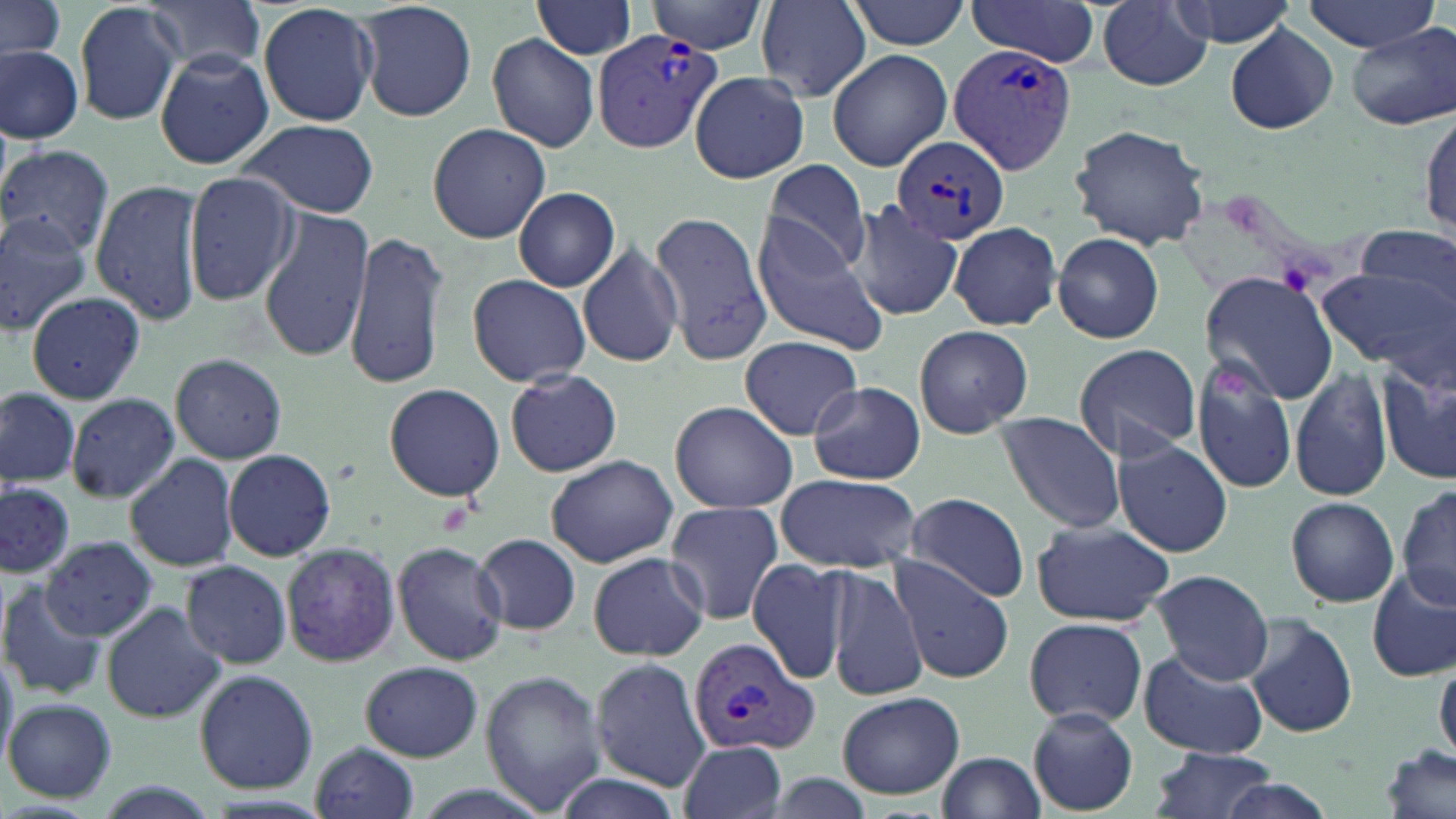

slide_level_diagnosis: Plasmodium vivax
stain: May-Grünwald-Giemsa
magnification: 1000x
preparation: thin blood film
uninfected_red_blood_cell_locations: 'approximate bounding boxes as (x1, y1, x2, y2) in pixels: (1, 0, 67, 63), (354, 0, 477, 121), (756, 0, 872, 100), (1166, 0, 1298, 47), (75, 1, 184, 126), (534, 1, 639, 60), (647, 1, 768, 52), (847, 1, 973, 51), (963, 1, 1103, 66), (1092, 1, 1217, 92), (1301, 1, 1440, 53), (145, 2, 266, 75), (258, 2, 379, 128), (92, 22, 232, 161), (1225, 23, 1339, 134), (1348, 26, 1455, 128), (487, 33, 599, 152), (1, 45, 83, 143), (826, 47, 951, 173), (155, 50, 273, 168), (690, 71, 809, 184), (1418, 105, 1455, 241), (236, 119, 379, 217), (426, 122, 549, 244), (1068, 123, 1211, 248), (0, 144, 116, 257), (763, 157, 873, 273), (183, 171, 299, 306), (90, 177, 206, 326), (514, 187, 621, 291), (849, 198, 963, 326), (259, 207, 372, 361), (651, 209, 772, 367), (0, 213, 92, 336), (750, 216, 889, 353), (949, 221, 1063, 330), (1357, 225, 1453, 311), (344, 229, 450, 392), (1052, 231, 1165, 345), (577, 240, 684, 367), (1317, 266, 1450, 373), (467, 274, 593, 386), (1200, 274, 1337, 403), (26, 292, 144, 404), (914, 324, 1035, 438), (738, 335, 865, 440), (1072, 342, 1201, 460), (1377, 348, 1456, 491), (1189, 352, 1301, 496), (169, 353, 288, 462), (1290, 365, 1392, 502), (504, 367, 622, 477), (808, 381, 924, 485), (381, 383, 506, 501), (0, 385, 81, 487), (66, 392, 181, 502), (669, 400, 799, 513), (996, 413, 1126, 535), (1115, 440, 1234, 557), (223, 449, 336, 562), (124, 451, 239, 573), (544, 454, 678, 569), (774, 472, 920, 571), (0, 483, 77, 580), (1398, 483, 1456, 612), (903, 492, 1029, 602), (1284, 497, 1398, 606), (662, 503, 784, 625), (1030, 520, 1172, 628), (474, 534, 582, 636), (41, 536, 157, 640), (280, 540, 401, 668), (390, 540, 508, 665), (587, 552, 709, 661), (746, 558, 852, 684), (889, 558, 1015, 684), (181, 561, 292, 669), (824, 564, 927, 702), (1368, 569, 1456, 681), (1149, 570, 1275, 685), (0, 582, 108, 701), (100, 602, 226, 723), (1245, 614, 1357, 738), (1023, 616, 1149, 727), (1138, 650, 1270, 758), (591, 657, 709, 791), (360, 662, 483, 761), (1435, 662, 1456, 759), (192, 669, 319, 793), (478, 670, 607, 815), (837, 691, 965, 800), (5, 698, 117, 802), (1027, 708, 1138, 814), (677, 738, 788, 819), (309, 742, 419, 819), (1380, 745, 1453, 819), (1149, 746, 1278, 817), (937, 750, 1045, 817)'
plasmodium_vivax_infected_red_blood_cell_locations: 'approximate bounding boxes as (x1, y1, x2, y2) in pixels: (594, 30, 726, 154), (947, 43, 1078, 177), (895, 136, 1010, 246), (687, 634, 819, 757)'
image_size: 1456×819 pixels
platelet_locations: 'approximate bounding boxes as (x1, y1, x2, y2) in pixels: (1275, 257, 1319, 297), (1212, 369, 1249, 402)'
modality: optical microscopy
field_of_view: single